Assess this cell for malaria.
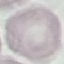
Uninfected.

Summary:
  - Image type: cell patch, automatically extracted from a larger field of view and resized to 64 × 64 pixels
  - Stain: Giemsa
  - Capture: smartphone through the microscope eyepiece
  - Preparation: thin smear